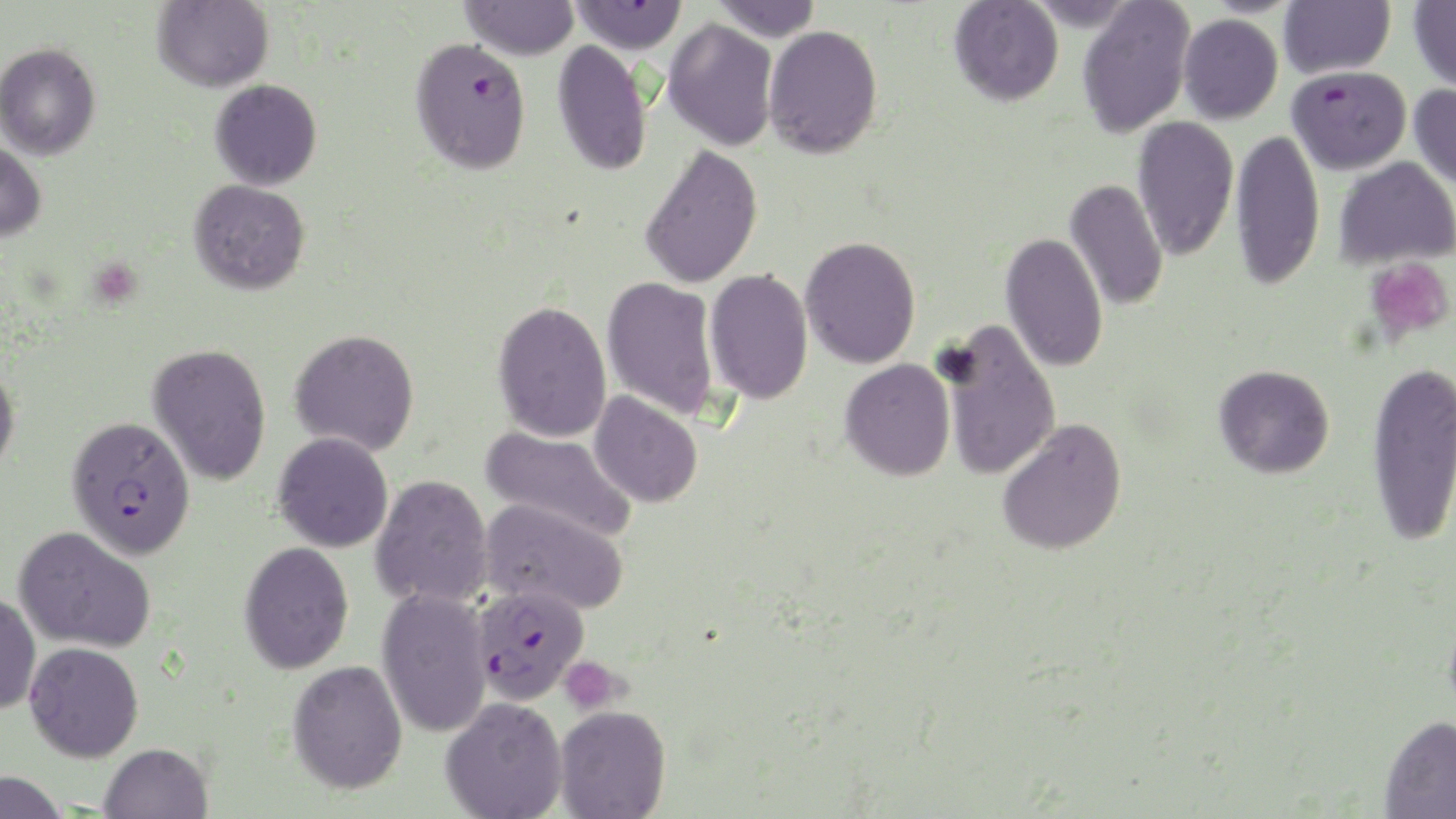

Summary:
  - Coordinate format: approximate bounding boxes as (x1, y1, x2, y2) in pixels
  - Uninfected red blood cell locations: (152, 0, 273, 92), (710, 0, 822, 41), (949, 0, 1063, 106), (1076, 0, 1195, 138), (1278, 0, 1395, 79), (1409, 0, 1456, 94), (459, 1, 580, 60), (1178, 14, 1283, 124), (662, 18, 778, 152), (763, 24, 884, 159), (552, 40, 653, 177), (0, 42, 101, 160), (210, 79, 322, 190), (1409, 84, 1456, 192), (1133, 116, 1238, 262), (1230, 129, 1324, 290), (0, 140, 47, 242), (639, 144, 763, 289), (1334, 156, 1456, 270), (1065, 178, 1168, 312), (188, 179, 310, 295), (1000, 232, 1108, 374), (800, 236, 921, 369), (704, 269, 813, 405), (602, 276, 721, 421), (492, 300, 613, 443), (938, 319, 1061, 481), (289, 328, 419, 456), (147, 343, 272, 486), (1366, 358, 1456, 547), (839, 359, 955, 481), (0, 362, 20, 478), (1214, 364, 1335, 478), (589, 391, 703, 508), (996, 418, 1127, 557), (480, 425, 638, 543), (272, 432, 393, 552), (370, 474, 493, 609), (480, 497, 629, 616), (14, 526, 156, 653), (239, 541, 354, 674), (376, 587, 493, 738), (0, 592, 41, 715), (24, 641, 144, 762), (287, 659, 408, 794), (440, 696, 567, 819), (554, 704, 671, 819), (1379, 714, 1456, 818), (99, 742, 212, 819), (0, 771, 69, 819)
  - Platelet locations: (1365, 257, 1455, 345), (558, 656, 625, 715)
  - Plasmodium falciparum-infected red blood cell locations: (569, 0, 687, 53), (409, 36, 531, 176), (1286, 66, 1411, 175), (67, 420, 198, 565), (472, 584, 589, 705)
  - Slide-level diagnosis: Plasmodium falciparum
  - Preparation: thin blood film
  - Modality: light microscopy
  - Field of view: one of a larger specimen
  - Image size: 1456×819 pixels
  - Stain: May-Grünwald-Giemsa
  - Magnification: 1000x